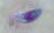
Summary:
  - Identification: Toxoplasma gondii
  - Modality: photomicrograph
  - Magnification: 1000x